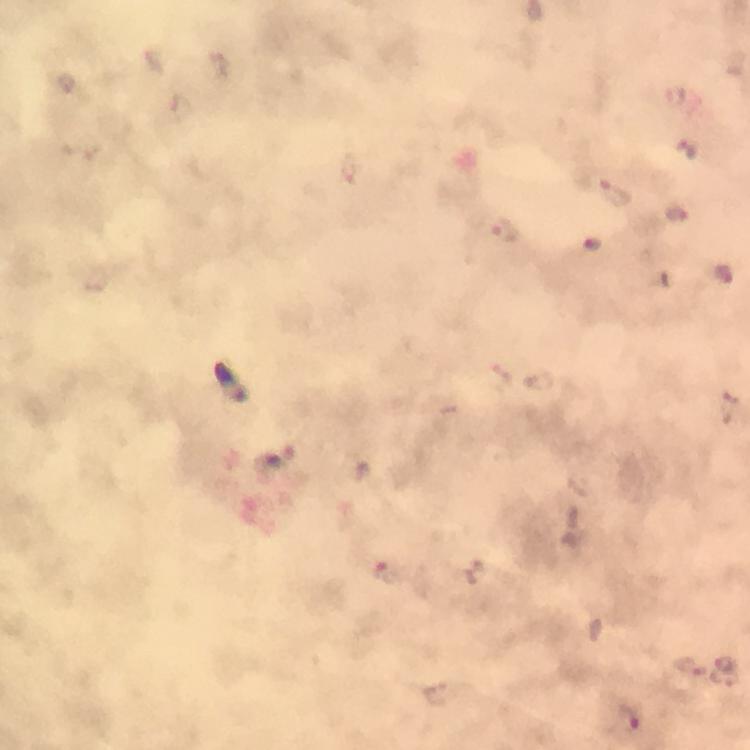

Approximate centers as [x, y] in pixels. Plasmodium parasite locations: [687, 150], [351, 167], [617, 193], [676, 212], [505, 230], [593, 244], [724, 275], [389, 571], [692, 666], [629, 717]. 100x magnification. Immersion oil applied. From a malaria diagnostic workup. Image is 750×750 pixels. Photographed with a smartphone mounted on the microscope. Giemsa-stained preparation. Thick smear. A crop from one field of view.